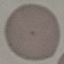
malaria status = uninfected
image type = automatically extracted cell patch, resized to 64 × 64 pixels
capture = smartphone through the microscope eyepiece
stain = Giemsa
preparation = thin blood film